Assess the morphology of the red blood cells.
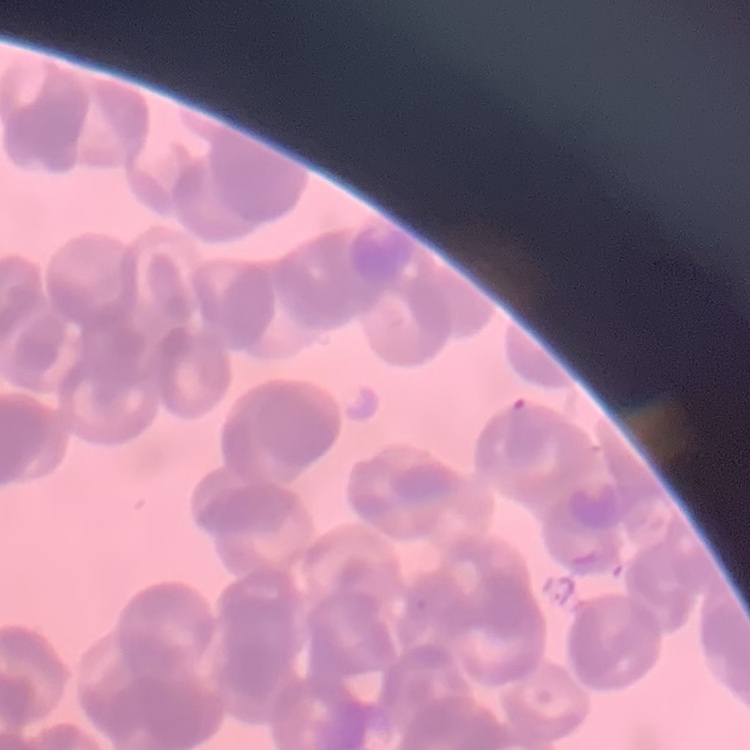
They show rouleaux formation.

Thin blood film. One tile cut from a larger photomicrograph. Stained with either Field's or Giemsa.